Classify this cell by malaria status.
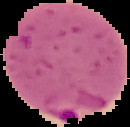

It is parasitized.

Image is 130×127 pixels. The area outside the segmented cell region is set to black. From a thin blood film.